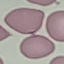
Summary:
  - Malaria status: uninfected
  - Preparation: thin blood smear
  - Capture: smartphone camera at the microscope eyepiece
  - Stain: Giemsa
  - Image type: cell patch, automatically extracted from a larger field of view and resized to 64 × 64 pixels